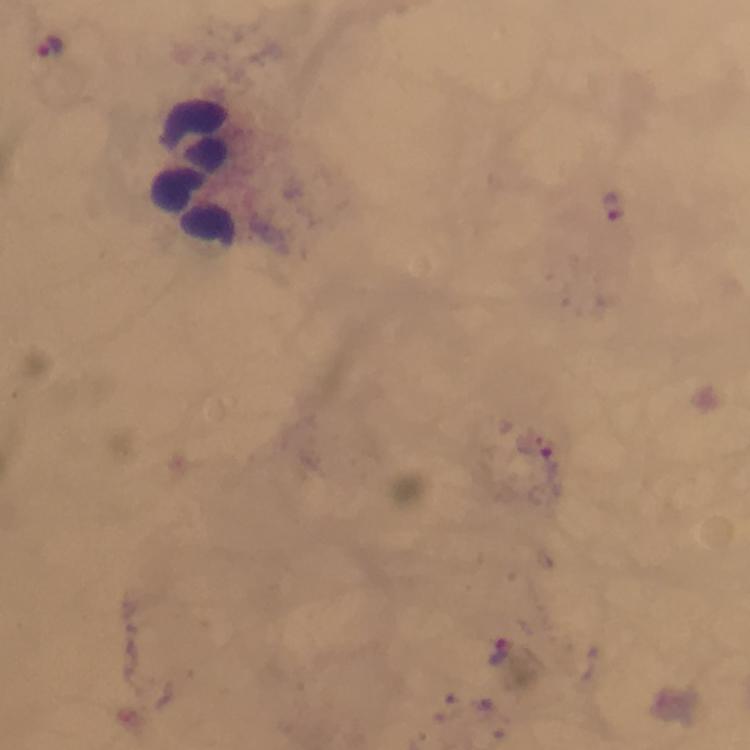
Approximate centers as {x, y} in pixels. Malaria parasite locations: {50, 44}, {616, 207}, {501, 652}. Leukocyte locations: {194, 173}. Giemsa stain. At 100x magnification. From a diagnostic examination for malaria. Image is 750×750 pixels. Cropped region of a single field of view. Thick smear. Immersion oil applied. Photographed through the microscope with a smartphone camera.